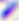
Summary:
  - Modality: micrograph
  - Identification: Toxoplasma gondii
  - Magnification: 400x